State which cell type is depicted.
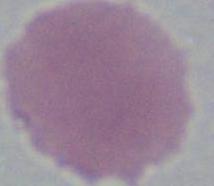
An erythrocyte.

Summary:
  - Magnification: 1000x
  - Modality: micrograph